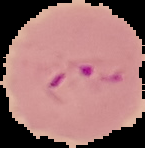
Result: malaria parasites detected. Cell region segmented out of the field of view; the surrounding area is masked to black. Image is 145×148 pixels. From a thin blood smear.